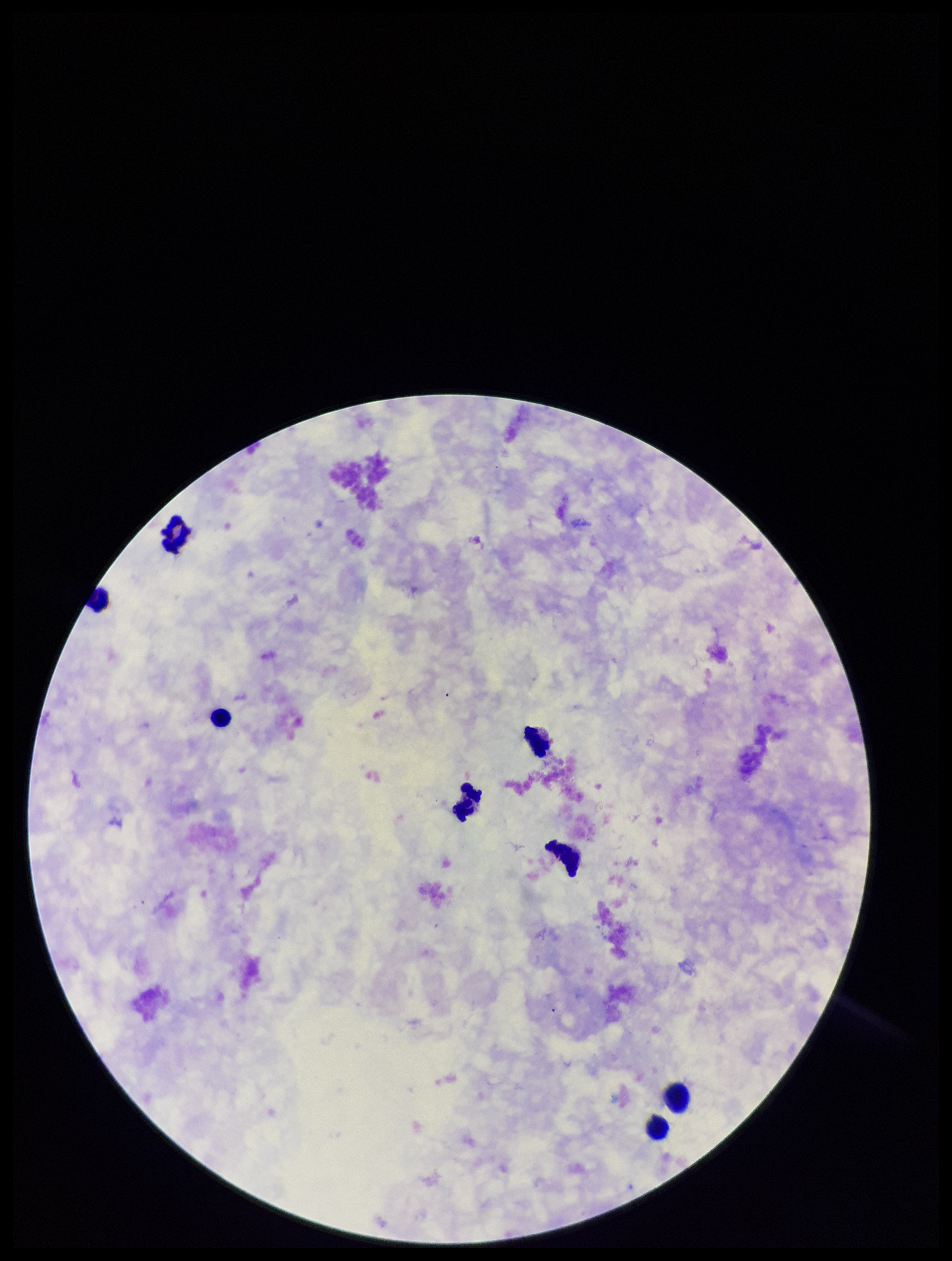

field of view = single
preparation = thick smear
Plasmodium parasites = none identified
leukocyte count = 8
patient malaria status = negative
image size = 952×1261 pixels
parasite count = 0
stain = Giemsa
capture = smartphone photograph through the microscope eyepiece